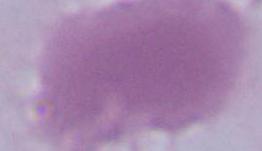

Summary:
  - Modality: micrograph
  - Magnification: 1000x
  - Identification: erythrocyte